Outline each blood parasite and name the species.
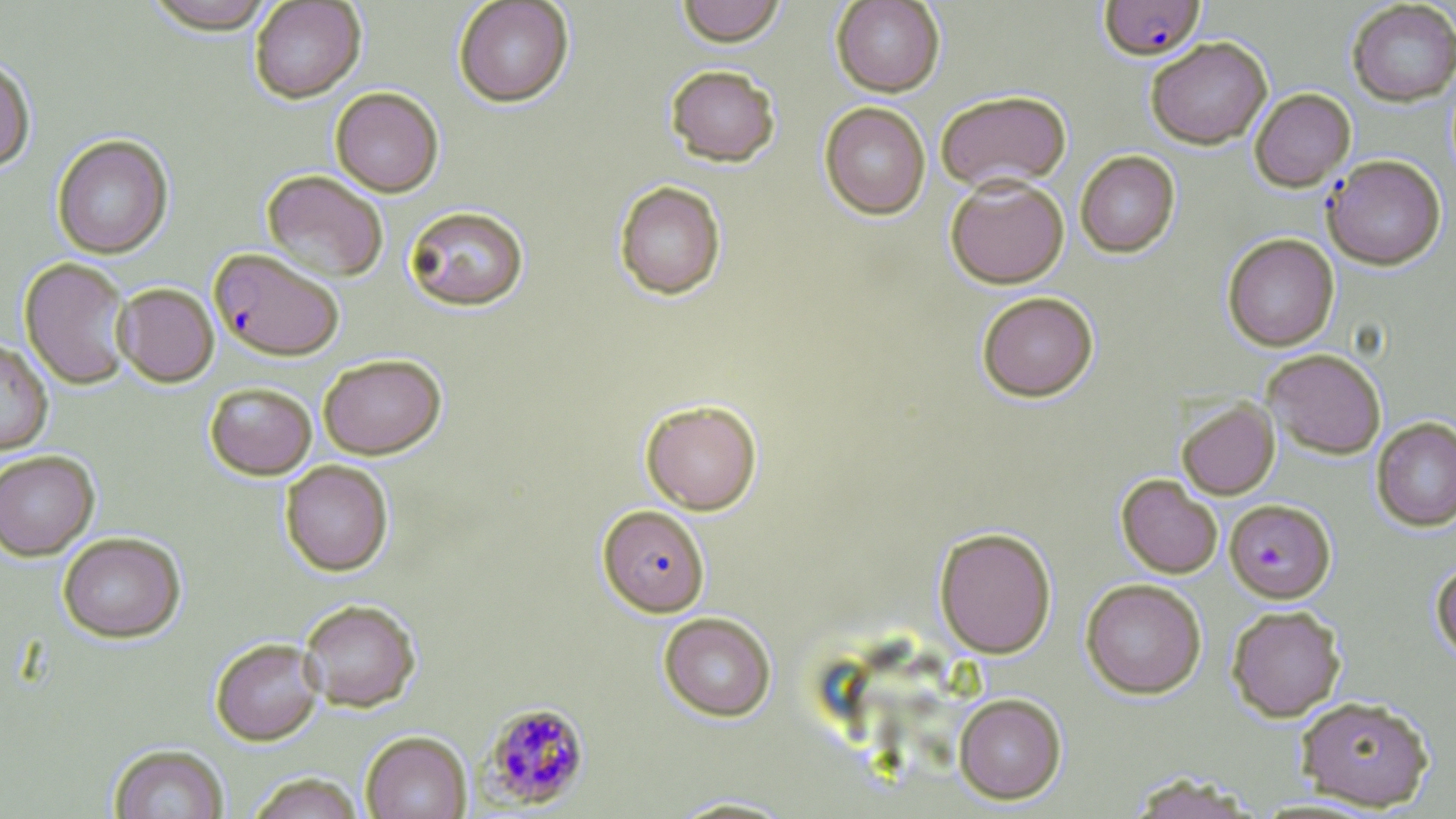
Approximate bounding boxes as [x1, y1, x2, y2] in pixels.
Plasmodium falciparum-infected red blood cells: [1099, 0, 1205, 59], [1323, 155, 1446, 270], [209, 247, 345, 361], [1225, 498, 1335, 602], [597, 504, 710, 617], [480, 702, 591, 810].
No Plasmodium ovale, Plasmodium malariae, Plasmodium vivax, Babesia divergens, or Trypanosoma brucei observed.

slide-level diagnosis = Plasmodium falciparum
preparation = thin blood smear
image size = 1456×819 pixels
modality = optical microscopy
field of view = one of a larger specimen
uninfected red blood cell locations = approximate bounding boxes as [x1, y1, x2, y2] in pixels: [141, 0, 279, 35], [249, 0, 366, 103], [453, 0, 574, 107], [676, 0, 785, 47], [831, 0, 945, 97], [1347, 1, 1456, 106], [1146, 37, 1272, 149], [0, 58, 35, 172], [664, 64, 780, 167], [330, 86, 444, 197], [1250, 88, 1355, 191], [935, 89, 1071, 191], [819, 102, 930, 219], [51, 134, 173, 259], [1075, 150, 1180, 257], [262, 170, 388, 282], [945, 176, 1069, 288], [614, 181, 726, 299], [403, 205, 530, 311], [1222, 233, 1339, 351], [19, 256, 133, 390], [113, 282, 219, 386], [977, 291, 1098, 401], [0, 339, 53, 456], [1263, 348, 1386, 459], [318, 353, 446, 459], [204, 381, 317, 480], [641, 399, 762, 514], [1177, 399, 1279, 499], [1371, 417, 1456, 531], [0, 450, 99, 561], [280, 459, 394, 576], [1116, 474, 1223, 578], [934, 527, 1056, 658], [57, 531, 186, 643], [1431, 559, 1456, 663], [1081, 578, 1206, 698], [298, 598, 421, 712], [1226, 604, 1346, 722], [659, 612, 776, 721], [210, 638, 324, 746], [954, 693, 1066, 803], [1296, 695, 1434, 811], [361, 730, 472, 819], [109, 744, 229, 819], [245, 772, 366, 819], [1124, 772, 1260, 819], [664, 795, 801, 818]
stain = May-Grünwald-Giemsa
magnification = 1000x